Classify this cell by malaria status.
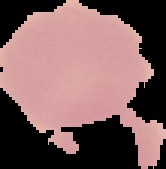

It is uninfected.

image type = cell region segmented out of the field of view; surrounding area masked to black
preparation = thin blood smear
image size = 166×169 pixels